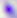

Summary:
  - Modality: photomicrograph
  - Magnification: 400x
  - Identification: Toxoplasma gondii